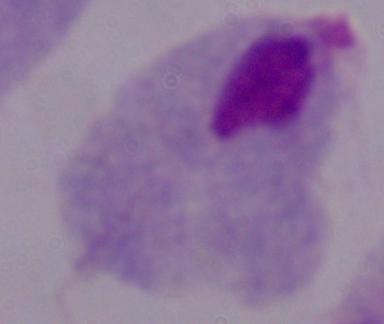

Summary:
  - Modality: micrograph
  - Identification: trichomonad
  - Magnification: 1000x